Locate every Plasmodium vivax-infected red blood cell.
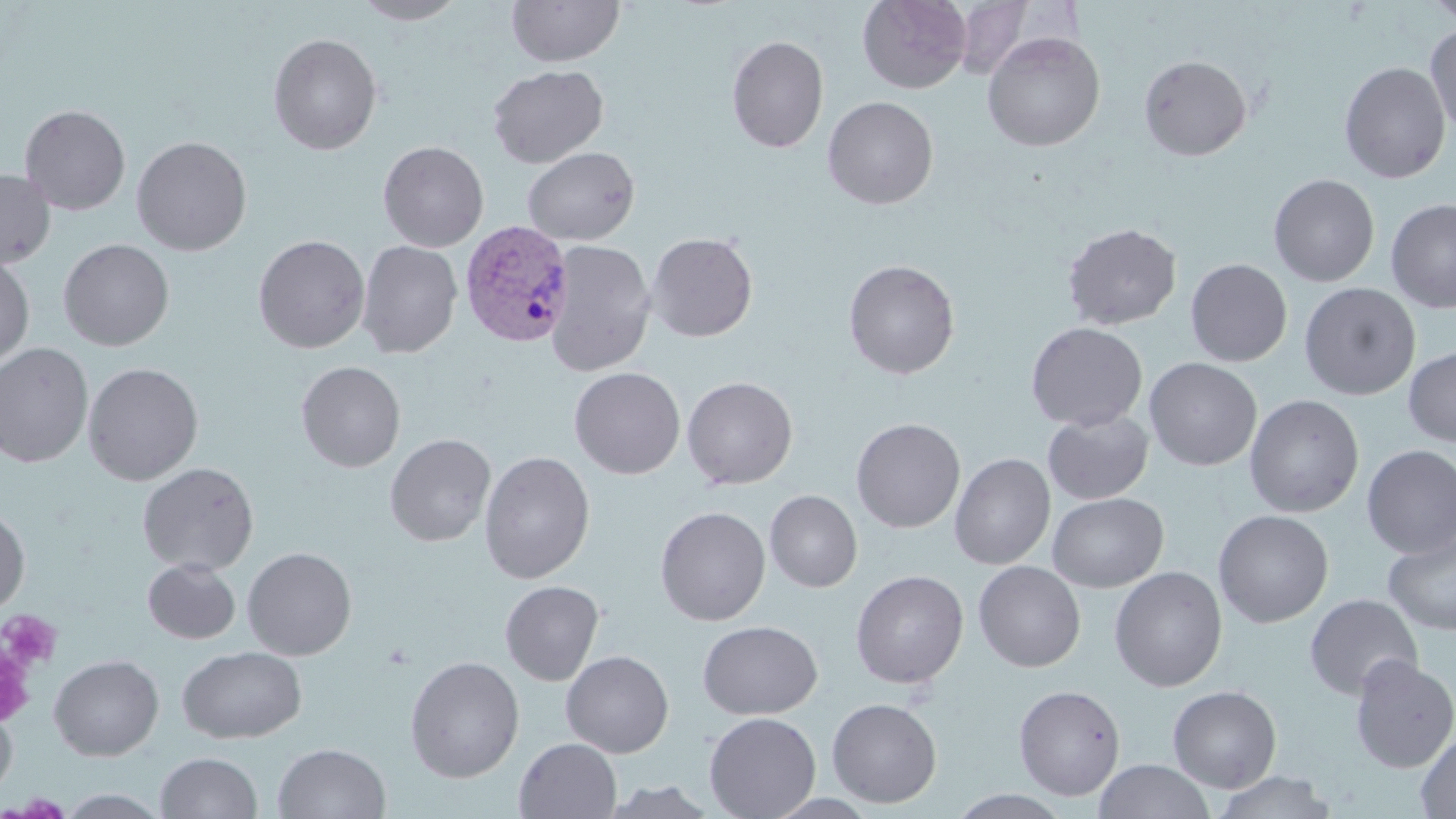

Approximate bounding boxes as named x1/y1/x2/y2 corners in pixels.
Plasmodium vivax-infected red blood cells: (x1=459, y1=219, x2=574, y2=346).

slide_level_diagnosis: Plasmodium vivax
modality: light microscopy
uninfected_red_blood_cell_locations: 'approximate bounding boxes as named x1/y1/x2/y2 corners in pixels: (x1=351, y1=0, x2=468, y2=25), (x1=506, y1=0, x2=625, y2=67), (x1=857, y1=0, x2=972, y2=93), (x1=1423, y1=0, x2=1456, y2=27), (x1=951, y1=1, x2=1036, y2=80), (x1=1425, y1=22, x2=1456, y2=138), (x1=981, y1=31, x2=1106, y2=152), (x1=267, y1=33, x2=383, y2=155), (x1=726, y1=35, x2=829, y2=153), (x1=1138, y1=55, x2=1252, y2=161), (x1=1339, y1=61, x2=1451, y2=183), (x1=488, y1=64, x2=609, y2=168), (x1=822, y1=96, x2=938, y2=210), (x1=19, y1=104, x2=131, y2=216), (x1=131, y1=135, x2=252, y2=255), (x1=378, y1=141, x2=489, y2=252), (x1=372, y1=143, x2=475, y2=361), (x1=522, y1=146, x2=640, y2=246), (x1=0, y1=169, x2=56, y2=268), (x1=1268, y1=173, x2=1380, y2=287), (x1=1385, y1=198, x2=1456, y2=313), (x1=1062, y1=223, x2=1182, y2=329), (x1=647, y1=232, x2=758, y2=342), (x1=253, y1=234, x2=370, y2=353), (x1=58, y1=238, x2=174, y2=351), (x1=357, y1=240, x2=462, y2=358), (x1=544, y1=240, x2=657, y2=376), (x1=0, y1=255, x2=35, y2=368), (x1=1185, y1=258, x2=1293, y2=366), (x1=842, y1=259, x2=961, y2=379), (x1=1299, y1=282, x2=1421, y2=400), (x1=1026, y1=322, x2=1147, y2=431), (x1=0, y1=342, x2=95, y2=468), (x1=1403, y1=344, x2=1456, y2=447), (x1=1144, y1=357, x2=1262, y2=471), (x1=296, y1=360, x2=406, y2=472), (x1=83, y1=362, x2=204, y2=485), (x1=569, y1=366, x2=686, y2=480), (x1=682, y1=376, x2=798, y2=490), (x1=1244, y1=394, x2=1364, y2=517), (x1=1043, y1=410, x2=1154, y2=504), (x1=851, y1=418, x2=965, y2=533), (x1=386, y1=433, x2=496, y2=546), (x1=1361, y1=445, x2=1456, y2=559), (x1=479, y1=451, x2=595, y2=583), (x1=950, y1=453, x2=1055, y2=570), (x1=137, y1=462, x2=260, y2=575), (x1=764, y1=490, x2=863, y2=592), (x1=1048, y1=492, x2=1168, y2=592), (x1=0, y1=505, x2=30, y2=616), (x1=656, y1=506, x2=771, y2=626), (x1=1213, y1=509, x2=1334, y2=628), (x1=1383, y1=530, x2=1456, y2=636), (x1=242, y1=547, x2=357, y2=660), (x1=142, y1=558, x2=241, y2=644), (x1=973, y1=561, x2=1086, y2=672), (x1=1109, y1=566, x2=1227, y2=692), (x1=851, y1=569, x2=968, y2=689), (x1=500, y1=580, x2=604, y2=685), (x1=1304, y1=593, x2=1422, y2=700), (x1=697, y1=620, x2=823, y2=719), (x1=177, y1=645, x2=307, y2=744), (x1=560, y1=650, x2=674, y2=757), (x1=48, y1=654, x2=164, y2=761), (x1=1349, y1=655, x2=1456, y2=773), (x1=405, y1=656, x2=524, y2=783), (x1=1014, y1=684, x2=1125, y2=800), (x1=1167, y1=685, x2=1282, y2=793), (x1=827, y1=698, x2=942, y2=807), (x1=0, y1=703, x2=17, y2=802), (x1=704, y1=712, x2=821, y2=819), (x1=1416, y1=727, x2=1456, y2=818), (x1=514, y1=737, x2=622, y2=819), (x1=272, y1=742, x2=391, y2=819), (x1=156, y1=752, x2=262, y2=818), (x1=1095, y1=760, x2=1215, y2=818), (x1=1210, y1=771, x2=1339, y2=818), (x1=598, y1=780, x2=720, y2=818), (x1=55, y1=789, x2=171, y2=818), (x1=947, y1=789, x2=1074, y2=818)'
preparation: thin blood smear
stain: May-Grünwald-Giemsa
image_size: 1456×819 pixels
magnification: 1000x
field_of_view: single
platelet_locations: 'approximate bounding boxes as named x1/y1/x2/y2 corners in pixels: (x1=1, y1=610, x2=62, y2=673), (x1=1, y1=629, x2=41, y2=731)'